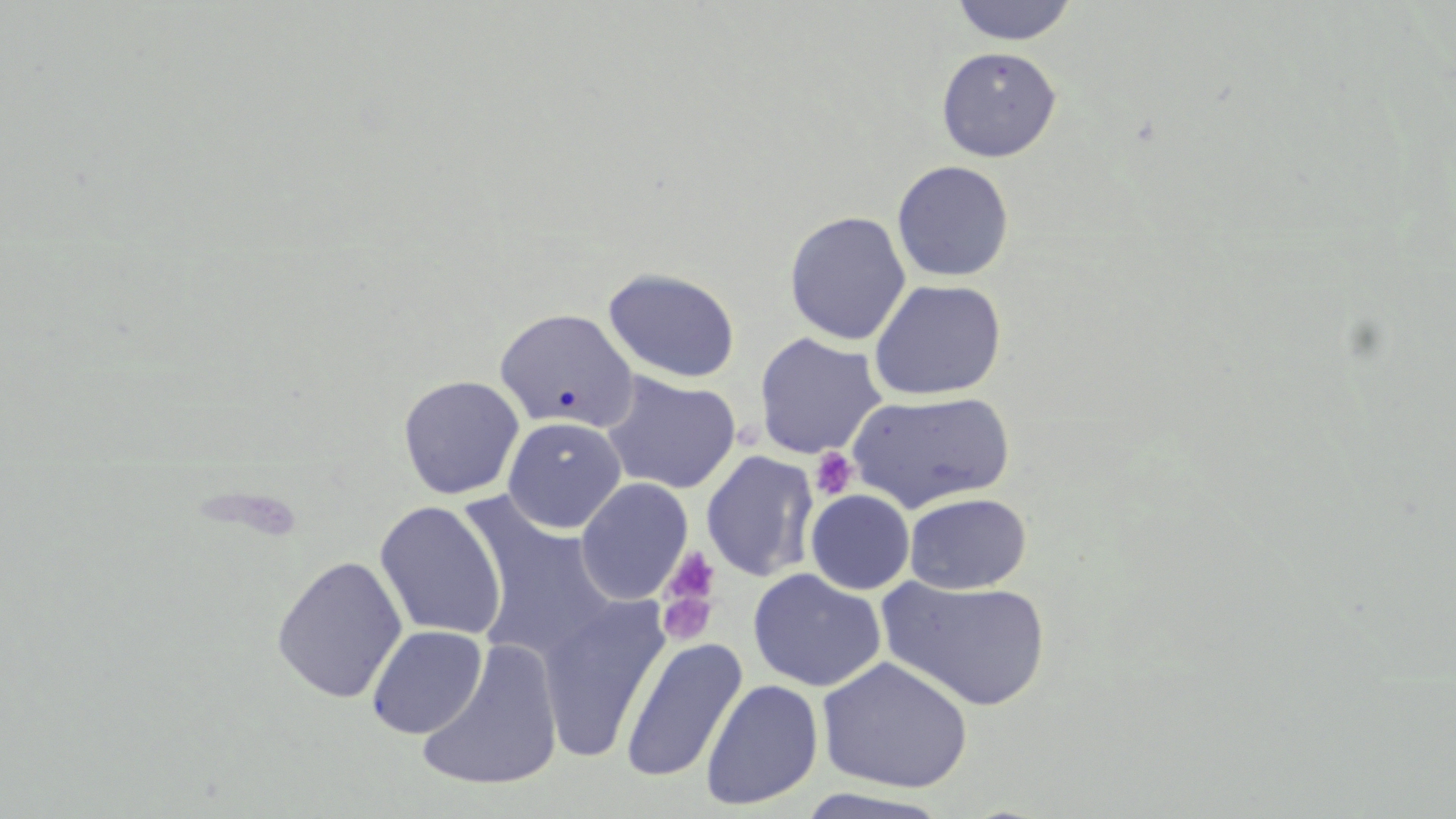

Summary:
  - Coordinate format: approximate bounding boxes as named x1/y1/x2/y2 corners in pixels
  - Platelet locations: (x1=811, y1=448, x2=857, y2=500), (x1=661, y1=546, x2=722, y2=615), (x1=655, y1=581, x2=719, y2=646)
  - Uninfected red blood cell locations: (x1=949, y1=0, x2=1078, y2=45), (x1=936, y1=46, x2=1062, y2=162), (x1=891, y1=160, x2=1014, y2=282), (x1=784, y1=211, x2=911, y2=345), (x1=603, y1=267, x2=741, y2=383), (x1=869, y1=278, x2=1007, y2=400), (x1=495, y1=308, x2=639, y2=432), (x1=753, y1=332, x2=886, y2=460), (x1=602, y1=372, x2=741, y2=495), (x1=398, y1=375, x2=525, y2=499), (x1=847, y1=390, x2=1016, y2=513), (x1=502, y1=416, x2=626, y2=533), (x1=700, y1=450, x2=820, y2=582), (x1=575, y1=477, x2=693, y2=605), (x1=805, y1=489, x2=915, y2=594), (x1=904, y1=492, x2=1031, y2=594), (x1=458, y1=495, x2=620, y2=667), (x1=374, y1=500, x2=507, y2=641), (x1=271, y1=554, x2=408, y2=704), (x1=748, y1=568, x2=886, y2=692), (x1=877, y1=576, x2=1052, y2=712), (x1=538, y1=594, x2=671, y2=764), (x1=367, y1=624, x2=486, y2=739), (x1=620, y1=637, x2=747, y2=784), (x1=415, y1=639, x2=565, y2=792), (x1=817, y1=655, x2=973, y2=794), (x1=700, y1=679, x2=824, y2=810), (x1=792, y1=788, x2=956, y2=819)
  - Slide-level diagnosis: negative for blood parasites
  - Stain: May-Grünwald-Giemsa
  - Modality: optical microscopy
  - Magnification: 1000x
  - Field of view: one of a larger specimen
  - Image size: 1456×819 pixels
  - Preparation: thin blood film